Name the parasite shown.
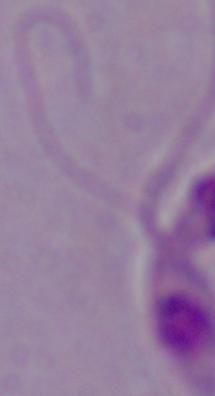
This is Leishmania.

modality = micrograph
magnification = 1000x